Identify the cell.
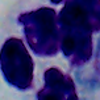

A leukocyte.

magnification = 1000x
modality = micrograph